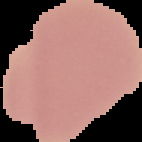

From a thin blood smear. Cell region segmented out of the field of view; the surrounding area is masked to black. Malaria status: uninfected. Image is 142×142 pixels.